Assess this cell for malaria.
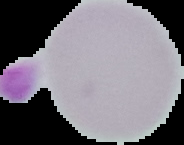

It is uninfected.

From a thin blood smear. Image is 184×145 pixels. Segmented cell region on a black background.